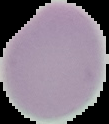 The area outside the segmented cell region is set to black. Result: no malaria parasites detected. Image is 109×124 pixels. From a thin blood smear.